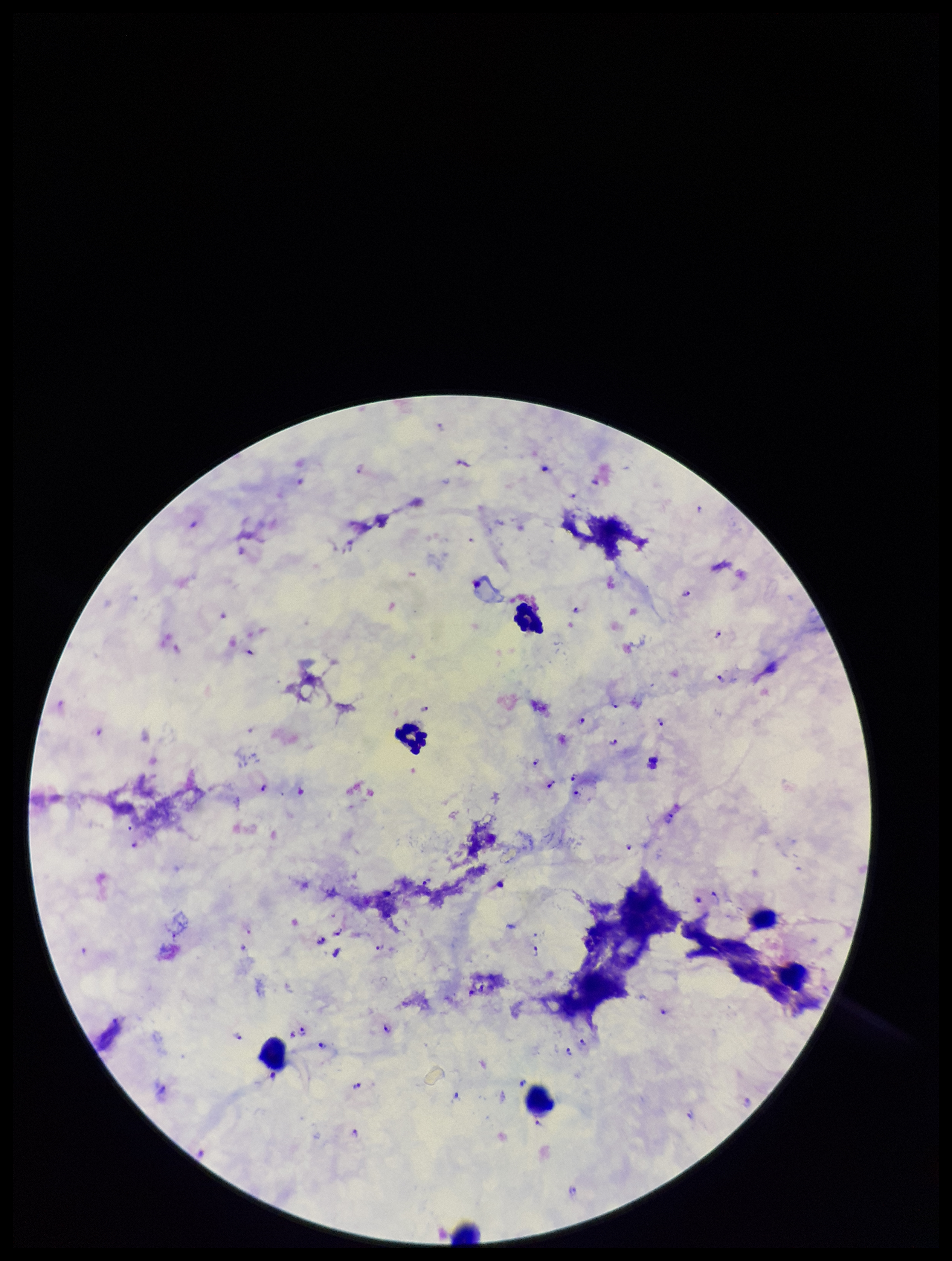
species_reported_for_this_patient: Plasmodium falciparum
stain: Giemsa
field_of_view: one from this slide
plasmodium_parasites: seen
image_size: 952×1261 pixels
leukocyte_count: 7
capture: smartphone photograph through the microscope eyepiece
patient_malaria_status: positive
preparation: thick blood smear
parasite_count: 31